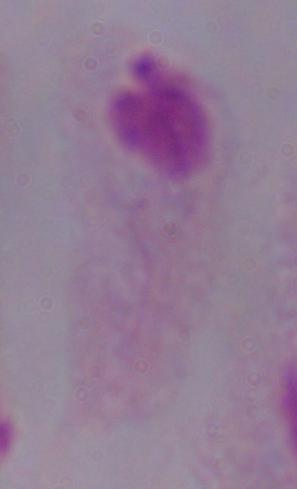

identification = trichomonad
magnification = 1000x
modality = micrograph